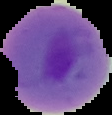
Cell region segmented out of the field of view; the surrounding area is masked to black. From a thin blood smear. Malaria status: parasitized. Image is 112×115 pixels.